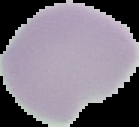
Summary:
  - Result: no Plasmodium parasites seen
  - Image size: 139×127 pixels
  - Image type: segmented cell region with the area outside set to black
  - Preparation: thin blood film